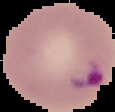

{
  "malaria_status": "parasitized",
  "image_type": "segmented cell region with the area outside set to black",
  "preparation": "thin blood film",
  "image_size": "115×112 pixels"
}